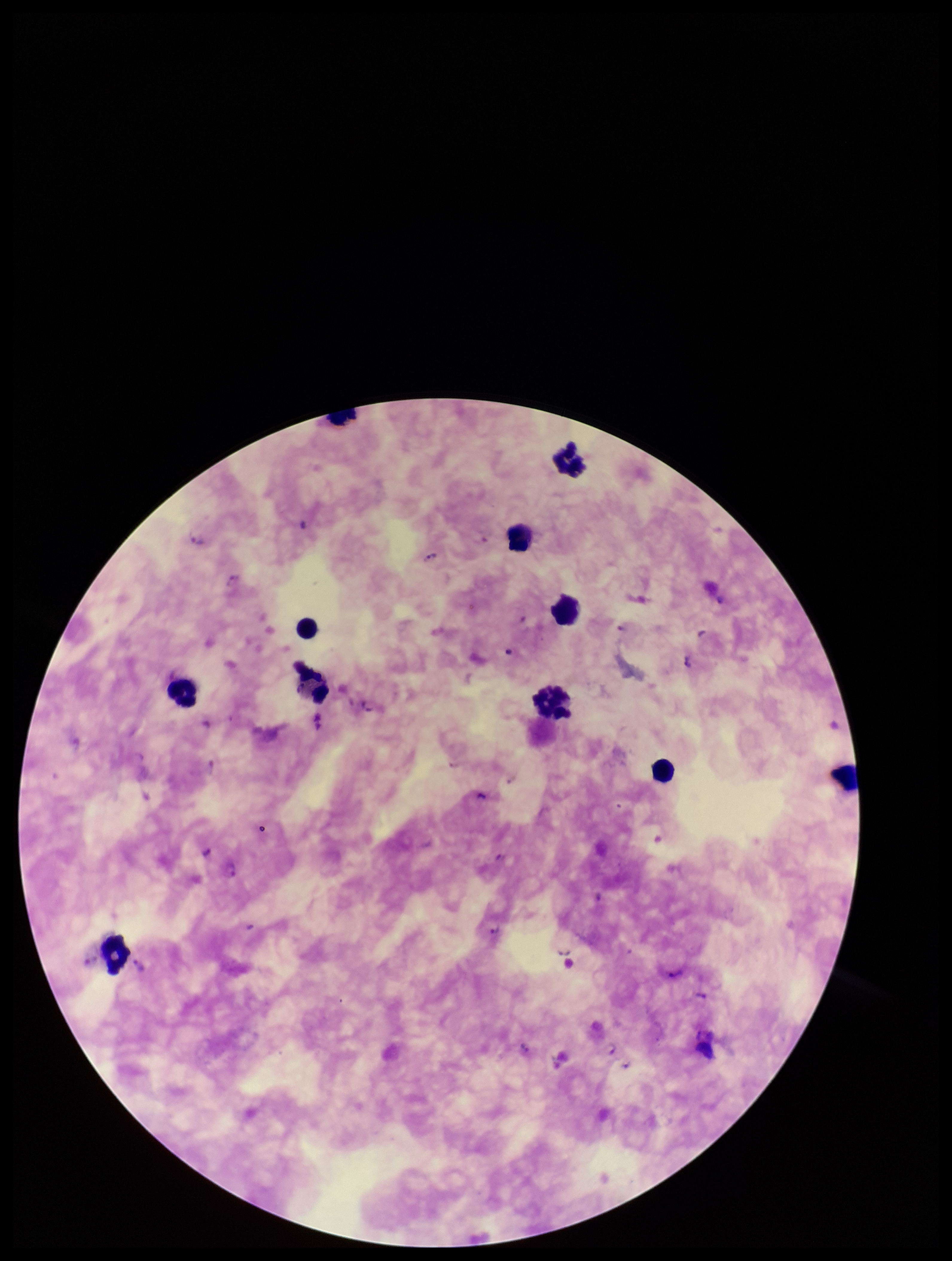

Summary:
  - Patient malaria status: infected
  - Field of view: one from this slide
  - Parasite count: 17
  - Species reported for this patient: Plasmodium falciparum
  - Stain: Giemsa
  - Preparation: thick blood smear
  - Plasmodium parasites: detected
  - Leukocyte count: 11
  - Image size: 952×1261 pixels
  - Capture: smartphone photograph through the microscope eyepiece